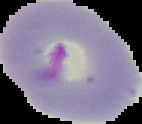
Summary:
  - Preparation: thin blood smear
  - Malaria status: parasitized
  - Image type: cell region segmented out of the field of view; surrounding area masked to black
  - Image size: 142×124 pixels